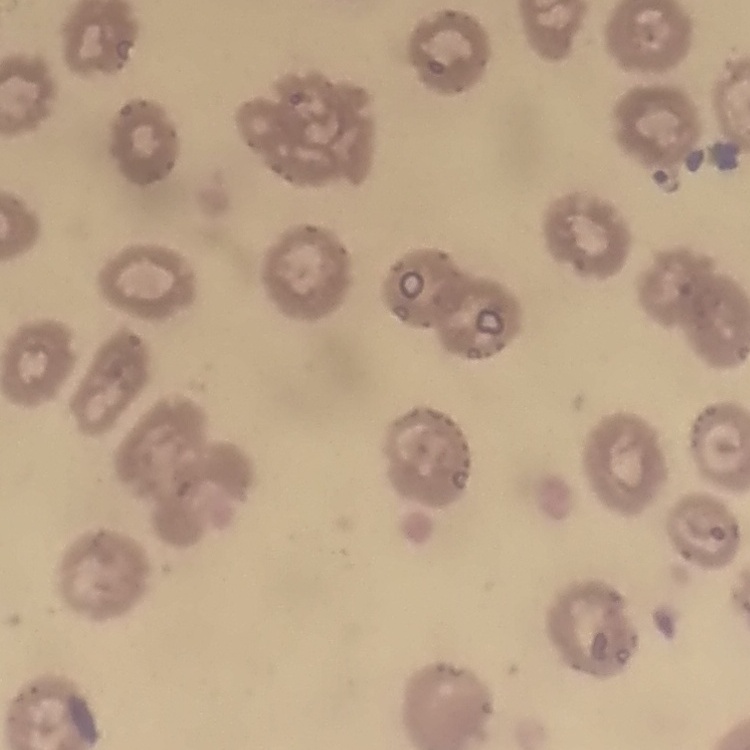

The red blood cells exhibit no rouleaux formation. Thin blood film. One tile cut from a larger photomicrograph. Field's or Giemsa stain.